Locate every Plasmodium parasite.
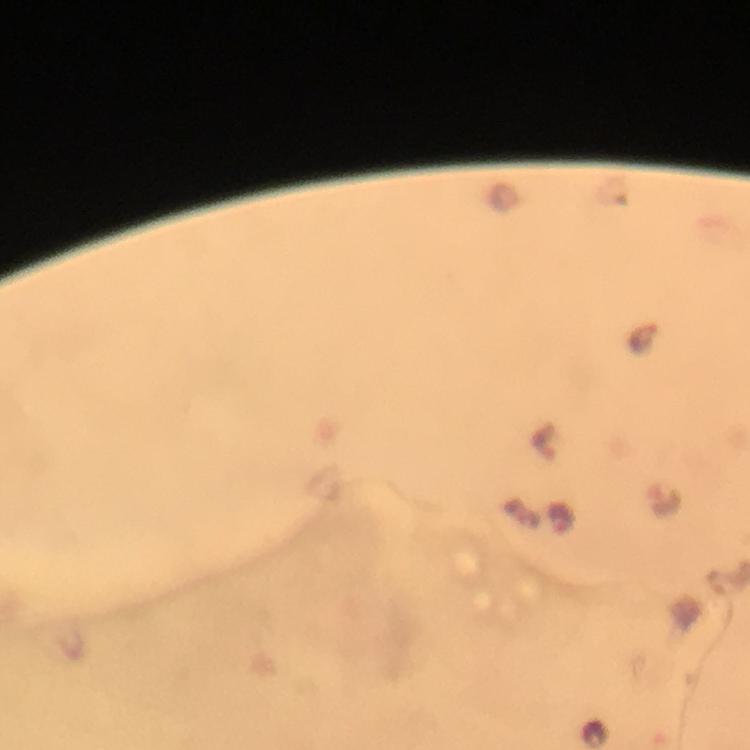
Approximate object centers, in pixels from the top-left corner.
Plasmodium parasites: (x=643, y=340), (x=543, y=441), (x=664, y=498), (x=561, y=518).

Image is 750×750 pixels. From a diagnostic examination for malaria. 100x magnification. Thick blood film. Immersion oil applied. Cropped region of a single field of view. Photographed with a smartphone mounted on the microscope. Giemsa stain.